Classify this cell by malaria status.
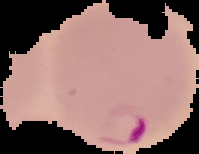
Parasitized.

Summary:
  - Image type: segmented cell region on a black background
  - Image size: 199×154 pixels
  - Preparation: thin blood film